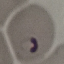
Summary:
  - Result: malaria parasites detected
  - Capture: smartphone through the microscope eyepiece
  - Preparation: thin blood smear
  - Image type: cell patch, automatically extracted from a larger field of view and resized to 64 × 64 pixels
  - Stain: Giemsa